Assess the morphology of the red blood cells.
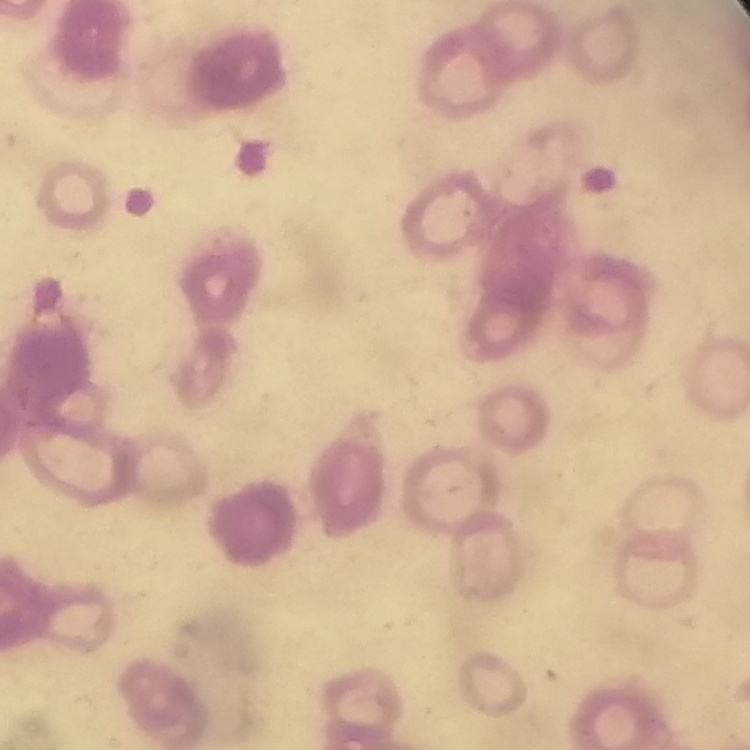
Rouleaux formation.

image_type: square crop of a larger photomicrograph
stain: Field's or Giemsa
preparation: thin blood smear